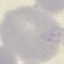

Malaria status: uninfected. Giemsa-stained preparation. Thin blood film. Automatically extracted cell patch, resized to 64 × 64 pixels. Acquired by smartphone through the microscope eyepiece.